Locate every leukocyte (white blood cell).
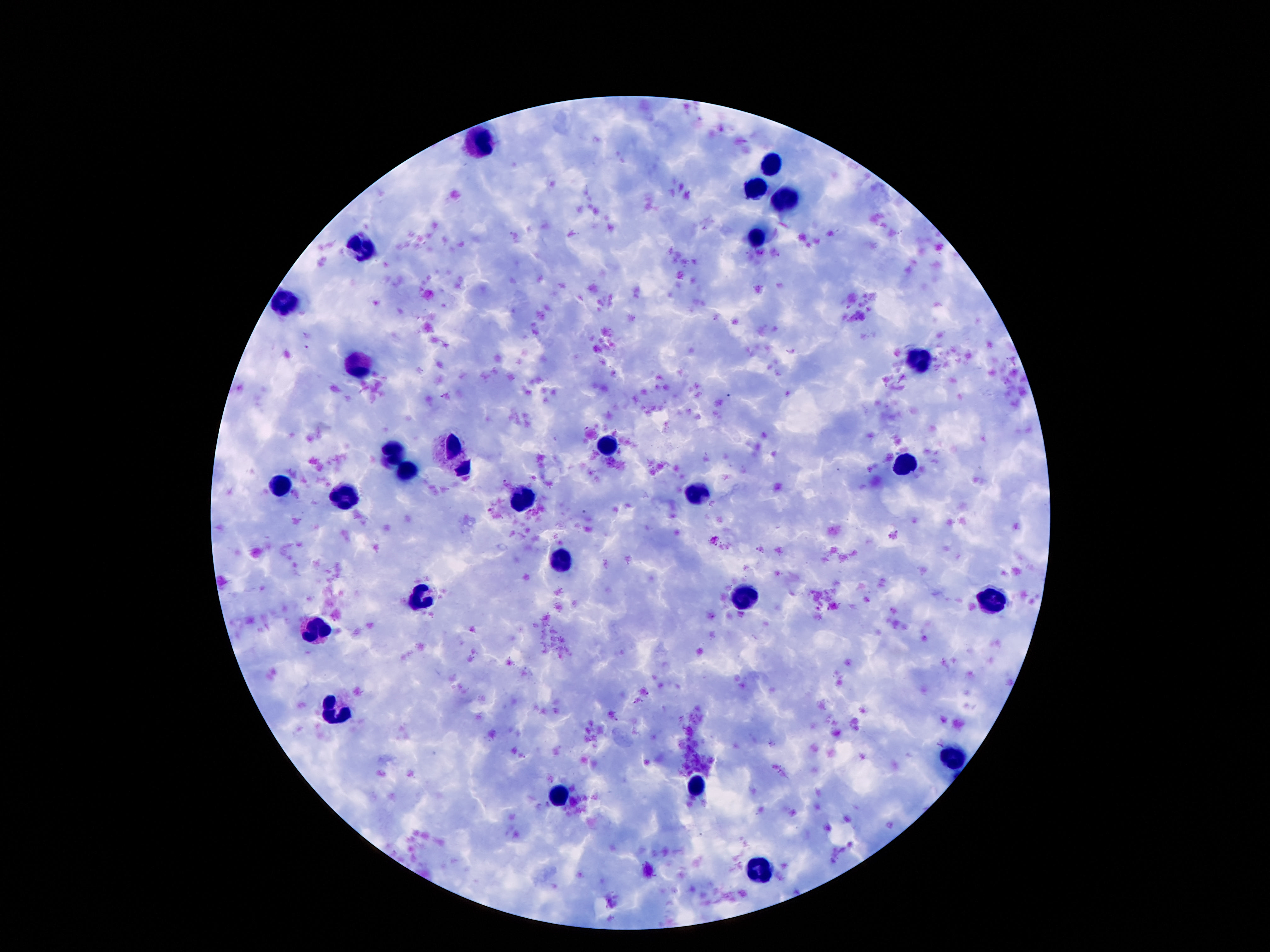
Approximate centers as {x, y} in pixels.
Leukocytes: {484, 142}, {774, 164}, {756, 188}, {783, 197}, {758, 236}, {363, 246}, {289, 302}, {916, 359}, {359, 363}, {606, 443}, {453, 446}, {395, 453}, {906, 466}, {408, 471}, {281, 485}, {701, 491}, {348, 496}, {520, 498}, {561, 558}, {424, 592}, {746, 596}, {990, 597}, {318, 631}, {332, 709}, {955, 756}, {699, 784}, {557, 795}, {760, 870}.

Summary:
  - Preparation: thick blood film
  - Patient malaria status: not infected
  - Field of view: one from this slide
  - Image size: 1270×952 pixels
  - Stain: Giemsa
  - Capture: smartphone camera through the microscope eyepiece
  - Magnification: 100x